State which parasite is depicted.
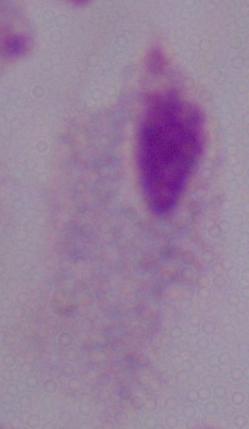
A trichomonad.

modality = micrograph
magnification = 1000x